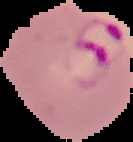 From a thin blood smear. Cell region segmented out of the field of view; the surrounding area is masked to black. Malaria status: parasitized. Image is 133×142 pixels.